Classify this cell by malaria status.
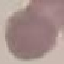
Uninfected.

capture = smartphone through the microscope eyepiece
stain = Giemsa
preparation = thin blood film
image type = automatically extracted cell patch, resized to 64 × 64 pixels